Classify this cell by malaria status.
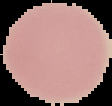

It is uninfected.

{
  "image_type": "cell region segmented out of the field of view; surrounding area masked to black",
  "image_size": "112×106 pixels",
  "preparation": "thin blood film"
}